Assess this cell for malaria.
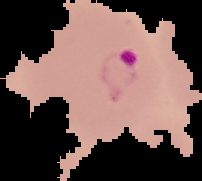
Parasitized.

{
  "image_size": "202×181 pixels",
  "image_type": "cell region segmented out of the field of view; surrounding area masked to black",
  "preparation": "thin blood smear"
}